Report the malaria status of this cell.
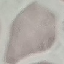

It is uninfected.

Summary:
  - Image type: cell patch, automatically extracted from a larger field of view and resized to 64 × 64 pixels
  - Preparation: thin blood smear
  - Stain: Giemsa
  - Capture: smartphone camera at the microscope eyepiece